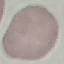

Summary:
  - Malaria status: uninfected
  - Preparation: thin smear
  - Image type: automatically extracted cell patch, resized to 64 × 64 pixels
  - Stain: Giemsa
  - Capture: smartphone camera at the microscope eyepiece